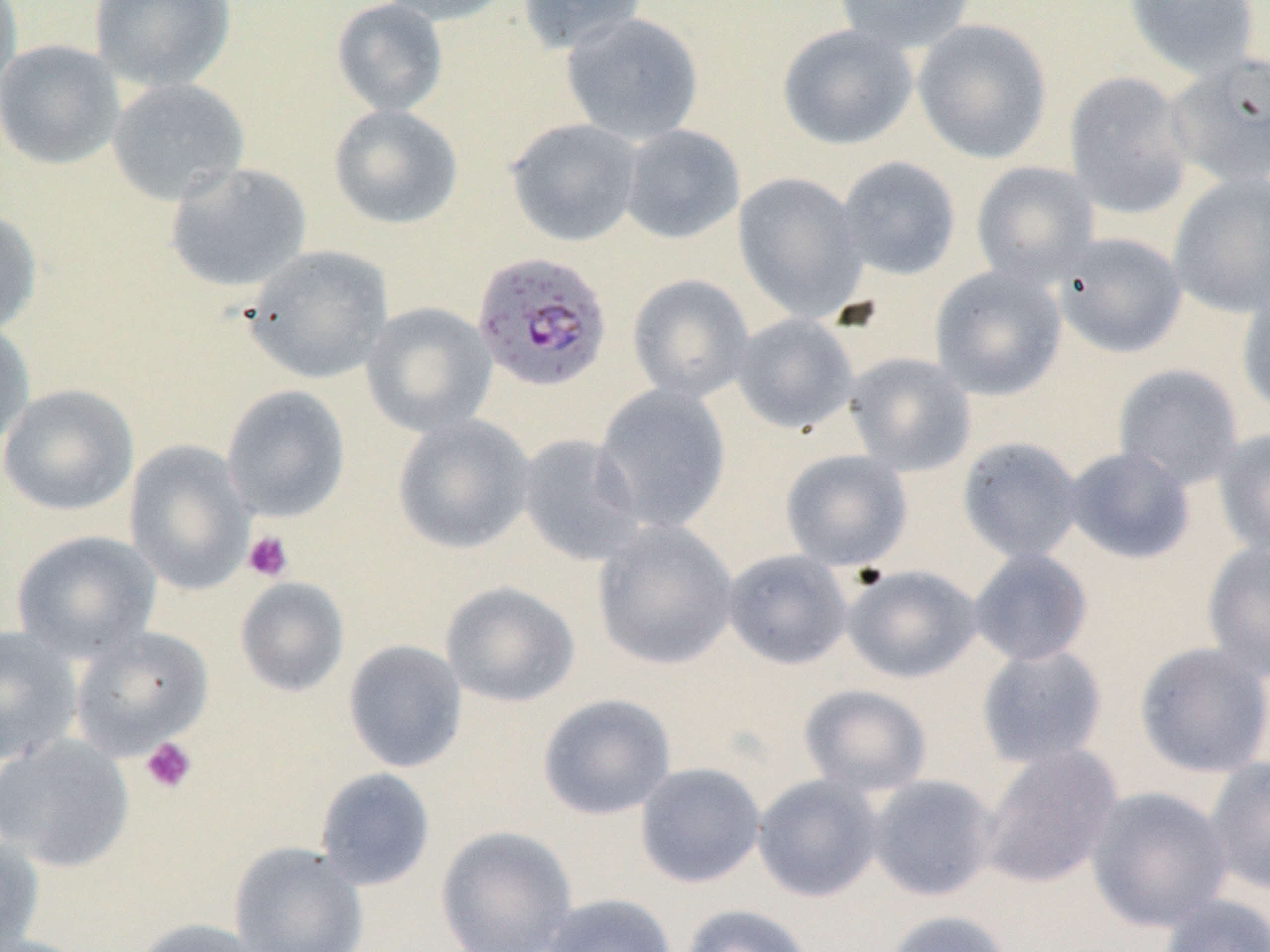

Summary:
  - Coordinate format: approximate bounding boxes as [x1, y1, x2, y2] in pixels
  - Platelet locations: [243, 530, 294, 582], [139, 736, 198, 795]
  - Uninfected red blood cell locations: [0, 0, 23, 96], [88, 0, 237, 92], [331, 0, 449, 117], [378, 0, 516, 26], [516, 0, 648, 53], [833, 0, 977, 53], [1123, 0, 1261, 81], [560, 12, 704, 145], [911, 18, 1053, 164], [776, 24, 918, 150], [0, 39, 126, 170], [1165, 52, 1270, 188], [1063, 71, 1195, 219], [107, 77, 250, 205], [328, 104, 464, 230], [505, 118, 644, 247], [620, 124, 746, 244], [836, 156, 961, 281], [164, 161, 313, 293], [970, 161, 1100, 288], [1167, 172, 1270, 318], [733, 173, 868, 323], [0, 207, 42, 337], [1054, 232, 1188, 359], [243, 244, 394, 384], [929, 265, 1067, 401], [627, 274, 755, 403], [1236, 286, 1270, 419], [361, 301, 497, 438], [731, 313, 860, 434], [0, 318, 35, 453], [844, 352, 976, 477], [1113, 363, 1245, 491], [0, 383, 139, 517], [221, 384, 351, 522], [593, 385, 731, 532], [392, 414, 536, 554], [1212, 428, 1270, 558], [516, 433, 646, 566], [956, 436, 1085, 565], [124, 440, 256, 594], [1063, 446, 1195, 565], [780, 449, 913, 571], [592, 519, 739, 670], [11, 529, 162, 662], [1201, 540, 1270, 682], [722, 549, 854, 670], [968, 549, 1093, 667], [843, 565, 983, 684], [234, 576, 350, 697], [440, 581, 580, 708], [0, 623, 83, 765], [69, 625, 214, 760], [342, 639, 468, 773], [1134, 641, 1270, 779], [975, 644, 1109, 768], [798, 684, 932, 797], [537, 693, 677, 820], [0, 734, 135, 872], [977, 744, 1123, 889], [1204, 756, 1270, 895], [634, 761, 766, 888], [314, 767, 436, 891], [752, 773, 884, 902], [866, 774, 1000, 902], [1085, 787, 1232, 932], [434, 826, 577, 952], [0, 832, 45, 952], [229, 841, 369, 952], [539, 892, 678, 952], [1158, 894, 1270, 952], [678, 903, 815, 952], [882, 909, 1016, 952], [128, 918, 269, 952]
  - Plasmodium falciparum-infected red blood cell locations: [472, 251, 613, 393]
  - Slide-level diagnosis: Plasmodium falciparum
  - Magnification: 1000x
  - Preparation: thin blood film
  - Stain: May-Grünwald-Giemsa
  - Field of view: one of a larger specimen
  - Modality: light microscopy
  - Image size: 1270×952 pixels